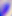

identification = Toxoplasma gondii
modality = photomicrograph
magnification = 400x